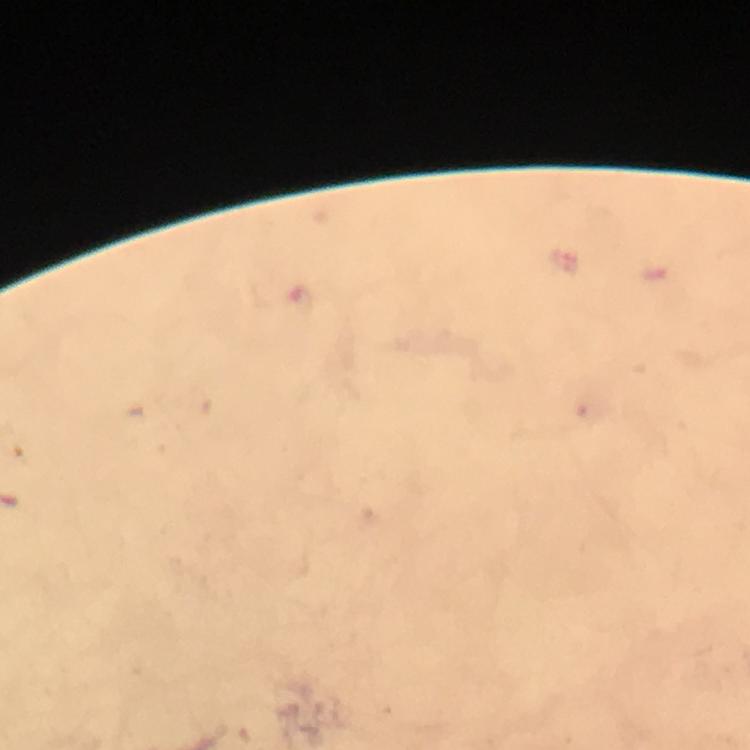

image_size: 750×750 pixels
immersion_oil: used
magnification: 100x
stain: Giemsa
preparation: thick blood film
malaria_parasite_locations: 'approximate object centers, in pixels from the top-left corner: (x=301, y=301)'
context: from a diagnostic examination for malaria
cropped_from: a single field of view
capture: smartphone camera through the microscope